Report the malaria status of this cell.
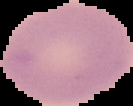

Uninfected.

Image is 133×106 pixels. From a thin blood film. Cell region segmented out of the field of view; the surrounding area is masked to black.